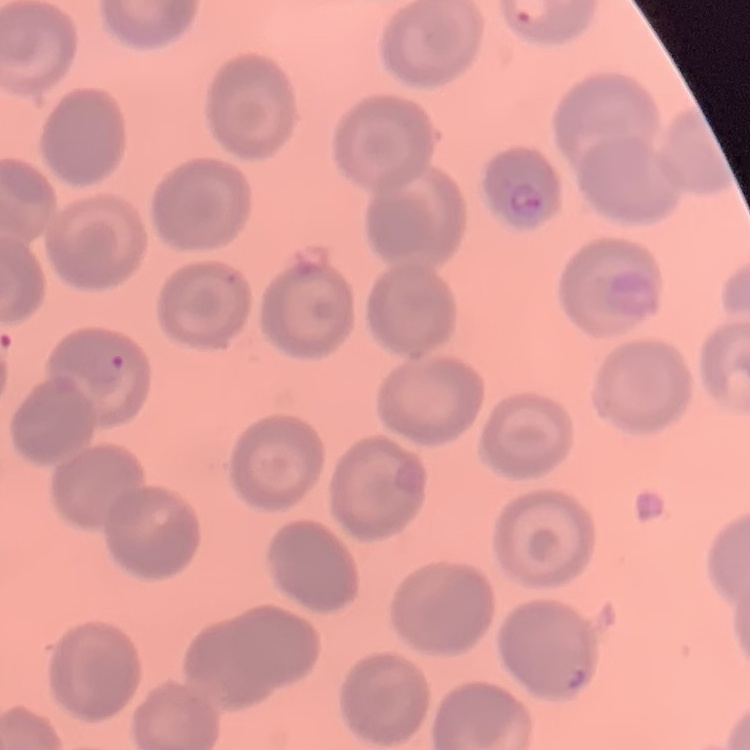
erythrocyte_morphology: no rouleaux formation
image_type: square crop of a larger photomicrograph
preparation: thin peripheral smear
stain: Field's or Giemsa